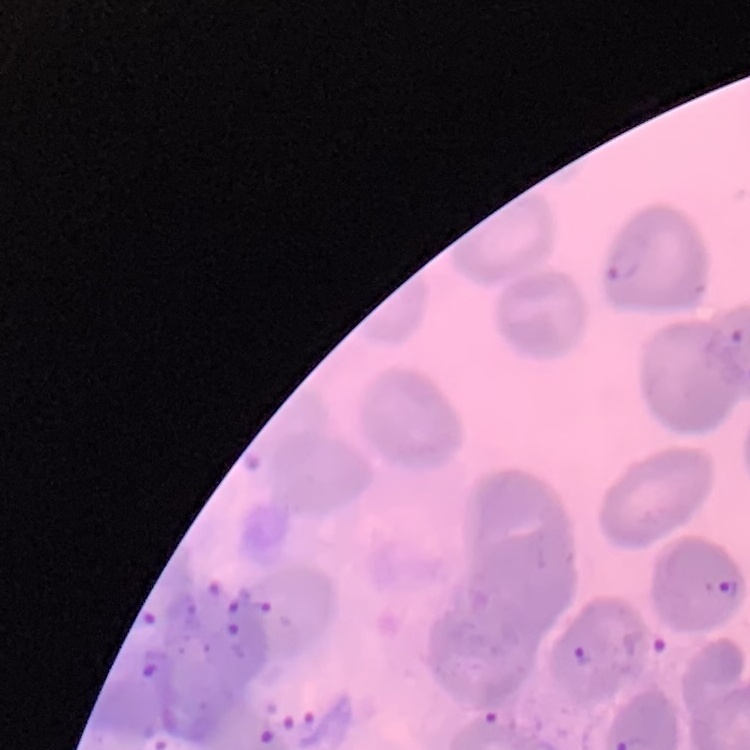
The erythrocytes exhibit no rouleaux formation. Thin blood smear. Stained with either Field's or Giemsa. One tile cut from a larger photomicrograph.